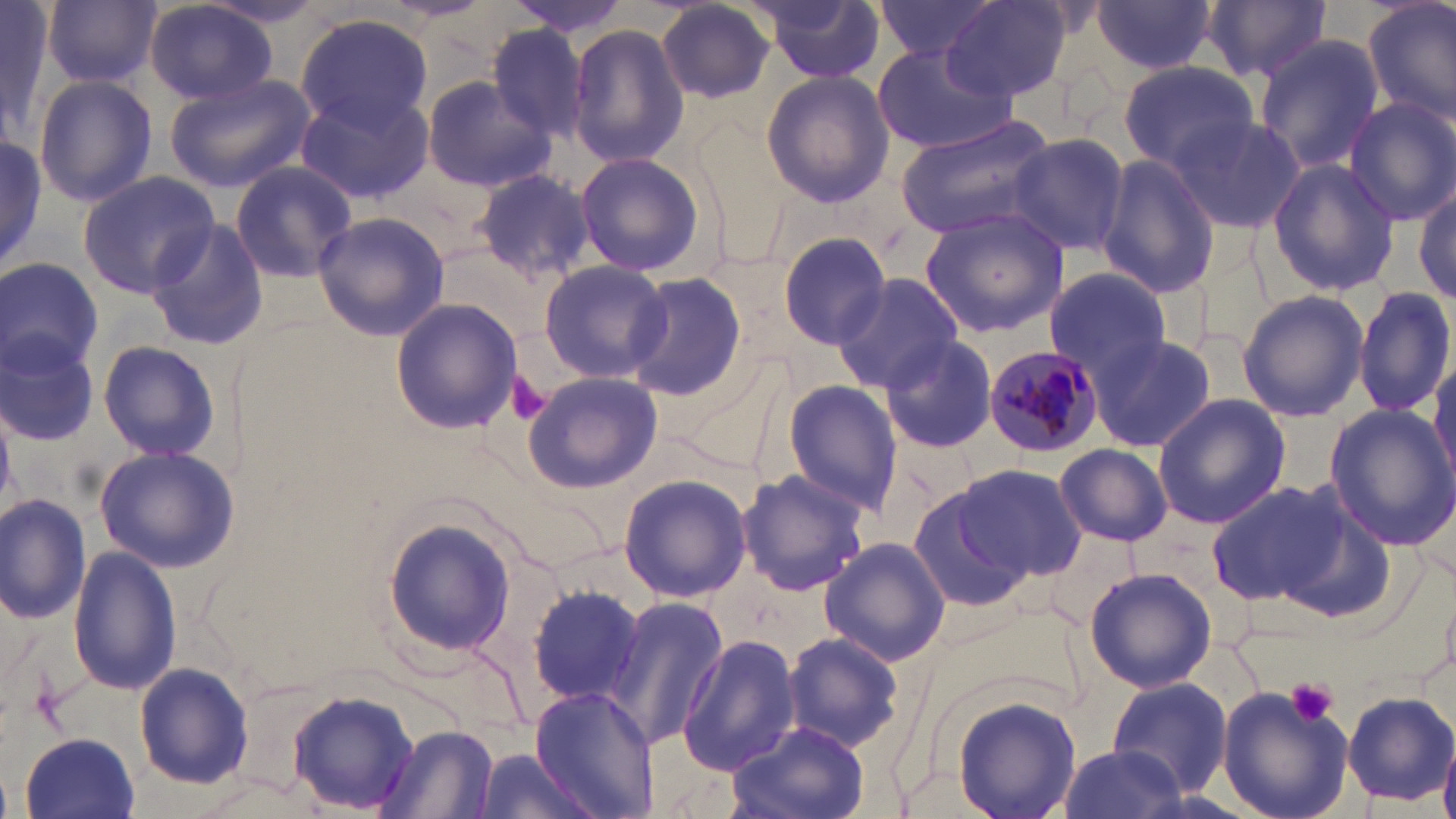

slide_level_diagnosis: Plasmodium malariae
magnification: 1000x
modality: optical microscopy
preparation: thin blood film
platelet_locations: 'approximate bounding boxes as (x1,y1)-(x2,y2) corner pairs in pixels: (506,371)-(551,426), (1284,676)-(1341,728)'
uninfected_red_blood_cell_locations: 'approximate bounding boxes as (x1,y1)-(x2,y2) corner pairs in pixels: (44,0)-(159,89), (500,0)-(639,38), (871,0)-(1004,65), (1093,0)-(1217,76), (1363,0)-(1456,127), (0,2)-(53,132), (145,2)-(278,106), (656,2)-(775,104), (752,2)-(887,84), (942,2)-(1071,102), (1201,2)-(1331,85), (296,12)-(435,131), (566,22)-(690,170), (487,23)-(590,140), (1253,34)-(1386,175), (873,43)-(1019,154), (1119,63)-(1261,172), (760,69)-(894,207), (32,73)-(156,209), (165,75)-(313,194), (419,76)-(554,193), (294,86)-(436,204), (1344,98)-(1455,225), (895,115)-(1057,239), (1170,115)-(1307,235), (0,134)-(48,272), (1008,135)-(1130,257), (575,151)-(708,279), (1096,154)-(1220,297), (1267,159)-(1399,296), (230,161)-(358,282), (472,169)-(595,284), (79,172)-(220,297), (1411,182)-(1456,311), (917,209)-(1069,338), (313,210)-(449,342), (142,217)-(269,353), (777,233)-(892,348), (0,256)-(103,380), (538,260)-(669,384), (1042,266)-(1174,380), (622,272)-(748,401), (831,272)-(965,393), (1353,285)-(1455,421), (1236,289)-(1368,422), (389,298)-(523,435), (0,329)-(103,449), (1087,332)-(1218,453), (878,334)-(998,454), (97,339)-(221,462), (1429,355)-(1456,486), (521,371)-(663,493), (782,380)-(903,516), (1153,395)-(1290,529), (1325,405)-(1456,549), (1057,444)-(1173,546), (92,445)-(238,574), (952,461)-(1088,583), (736,469)-(871,596), (618,473)-(749,602), (1206,478)-(1362,610), (905,481)-(1043,614), (0,493)-(90,627), (379,516)-(518,659), (818,536)-(952,665), (68,546)-(179,695), (1084,568)-(1217,693), (528,582)-(649,709), (607,594)-(732,751), (780,630)-(905,753), (677,635)-(802,772), (134,662)-(254,790), (1105,677)-(1233,797), (1215,681)-(1358,819), (529,686)-(656,819), (287,689)-(419,814), (1341,692)-(1454,804), (953,697)-(1082,819), (726,721)-(873,819), (377,725)-(500,818), (21,732)-(141,818), (1440,740)-(1456,819), (1058,745)-(1184,819), (470,749)-(596,819)'
plasmodium_malariae_infected_red_blood_cell_locations: 'approximate bounding boxes as (x1,y1)-(x2,y2) corner pairs in pixels: (982,342)-(1104,456)'
image_size: 1456×819 pixels
stain: May-Grünwald-Giemsa
field_of_view: one of a larger specimen